Classify this cell by malaria status.
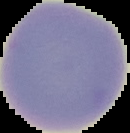
It is uninfected.

Image is 130×133 pixels. From a thin blood smear. Segmented cell region on a black background.